Identify the parasite.
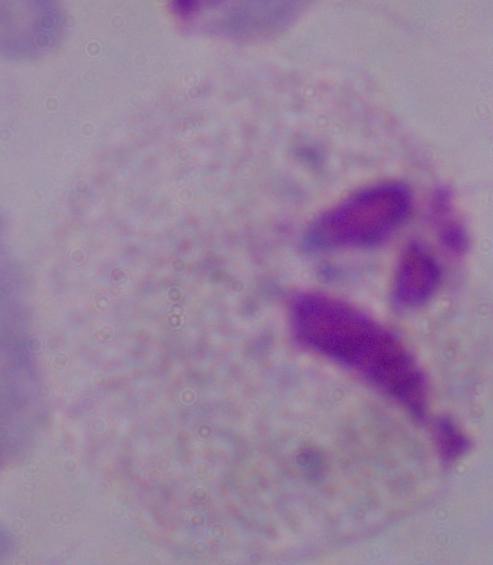

This is a trichomonad.

Captured at 1000x magnification. Photomicrograph.